Find the red blood cells that are infected with Plasmodium falciparum, and any of indeterminate infection status.
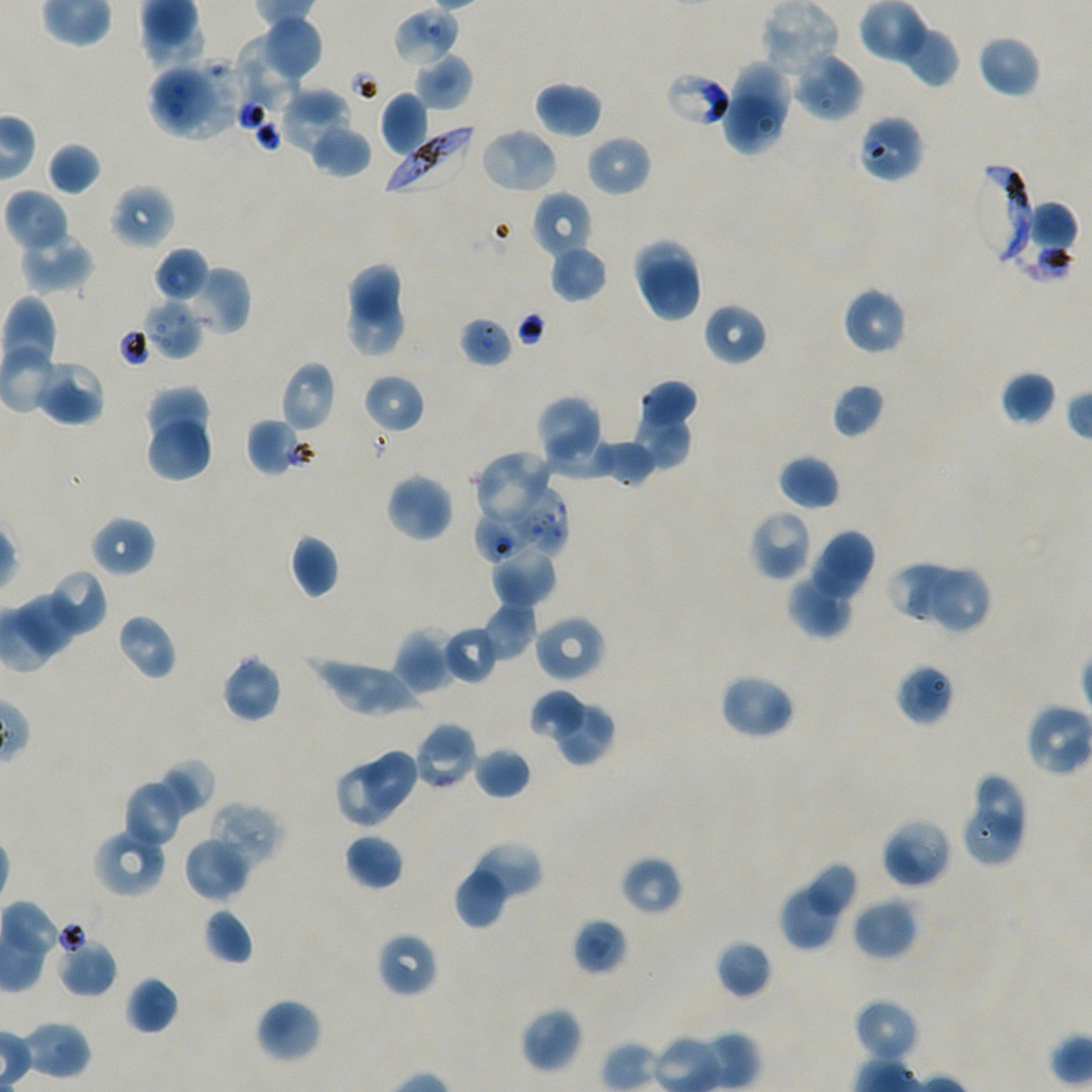
Approximate bounding boxes as (x1, y1, x2, y2) in pixels. Not every red blood cell is marked.
Infected red blood cells: (384, 128, 472, 193), (973, 166, 1032, 265).
Red blood cells of indeterminate infection status: (392, 6, 460, 67), (670, 77, 726, 124), (856, 114, 924, 183), (1003, 198, 1077, 281), (458, 315, 513, 368), (511, 485, 568, 557), (475, 508, 538, 562).

Summary:
  - Locations of uninfected red blood cells: (761, 0, 841, 79), (861, 0, 924, 59), (264, 15, 323, 77), (897, 22, 959, 88), (976, 34, 1042, 98), (238, 35, 302, 110), (792, 51, 863, 122), (416, 54, 473, 110), (730, 62, 790, 130), (147, 69, 213, 136), (534, 80, 603, 139), (282, 87, 350, 153), (380, 92, 429, 157), (725, 98, 781, 157), (309, 125, 372, 178), (479, 127, 560, 194), (585, 134, 652, 197), (46, 142, 102, 196), (109, 184, 175, 249), (532, 190, 594, 259), (4, 192, 67, 249), (19, 232, 94, 293), (636, 240, 695, 302), (154, 247, 210, 302), (551, 251, 606, 299), (644, 261, 699, 321), (349, 264, 400, 321), (184, 265, 250, 335), (841, 286, 909, 356), (1, 295, 55, 365), (349, 295, 405, 354), (144, 299, 204, 360), (702, 302, 768, 366), (33, 360, 106, 426), (279, 361, 335, 433), (1001, 371, 1057, 426), (362, 374, 424, 434), (637, 380, 697, 425), (831, 382, 885, 439), (145, 386, 211, 446), (534, 395, 604, 469), (637, 410, 691, 469), (150, 418, 209, 481), (248, 420, 298, 473), (549, 434, 609, 479), (592, 441, 652, 488), (477, 452, 551, 522), (778, 454, 839, 511), (385, 473, 454, 543), (752, 513, 810, 578), (90, 516, 156, 576), (812, 532, 875, 597), (290, 534, 340, 599), (492, 549, 556, 604), (890, 564, 962, 619), (45, 569, 108, 638), (931, 570, 987, 633), (786, 574, 850, 639), (18, 594, 77, 652), (481, 601, 537, 660), (116, 613, 178, 681), (533, 614, 606, 683), (442, 626, 500, 685), (393, 627, 455, 695), (221, 655, 283, 723), (304, 657, 423, 714), (894, 662, 956, 726), (723, 679, 790, 734), (531, 692, 581, 735), (557, 704, 616, 767), (415, 721, 478, 790), (473, 746, 532, 799), (366, 751, 417, 812), (160, 759, 215, 817), (337, 765, 393, 824), (978, 777, 1023, 841), (125, 785, 179, 843), (207, 801, 283, 871), (966, 813, 1018, 864), (884, 821, 949, 884), (94, 832, 164, 899), (344, 833, 404, 891), (183, 836, 251, 902), (468, 843, 542, 905), (620, 856, 682, 915), (810, 864, 856, 915), (456, 868, 506, 930), (782, 888, 837, 950), (852, 896, 918, 960), (202, 907, 255, 966), (572, 917, 629, 976), (376, 932, 439, 998), (56, 939, 117, 997), (714, 939, 773, 999), (126, 976, 179, 1035), (255, 997, 323, 1064), (853, 998, 920, 1064), (520, 1006, 583, 1073), (20, 1023, 88, 1077)
  - Image size: 1092×1092 pixels
  - Field of view: single
  - Preparation: thin blood film
  - Stain: Giemsa
  - Objective: 100x, oil immersion, numerical aperture 1.45
  - Donor blood group: A+/O+
  - Culture: Plasmodium falciparum strain NF54, static, in vitro